Name the cell type shown.
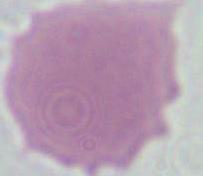
An erythrocyte.

Summary:
  - Magnification: 1000x
  - Modality: micrograph